Comment on the morphology of the red blood cells.
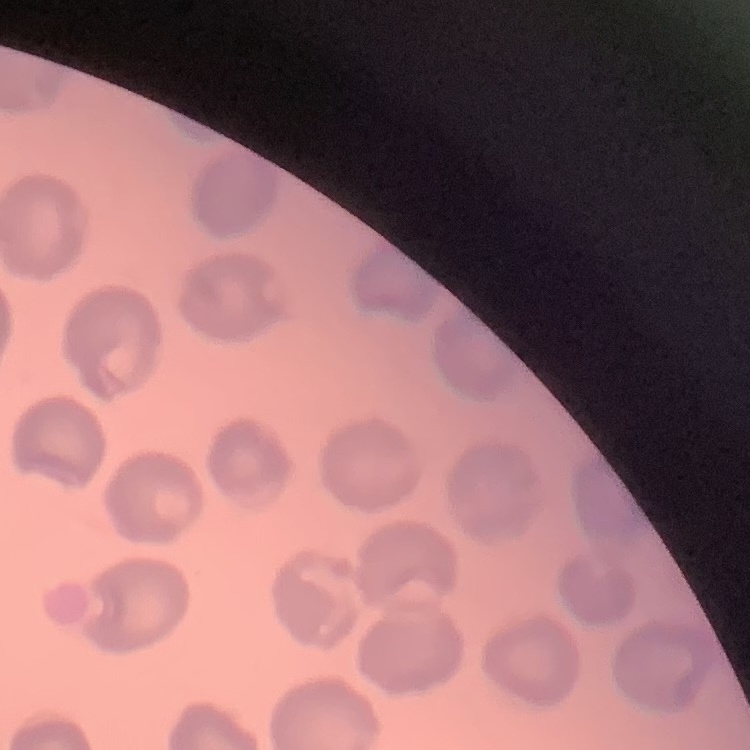

They show no rouleaux formation.

preparation = thin blood film
image type = one tile cut from a larger photomicrograph
stain = Field's or Giemsa